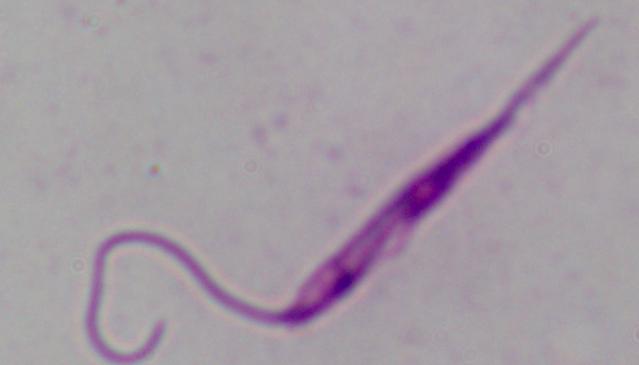

A Leishmania parasite is seen. Micrograph. 1000x magnification.